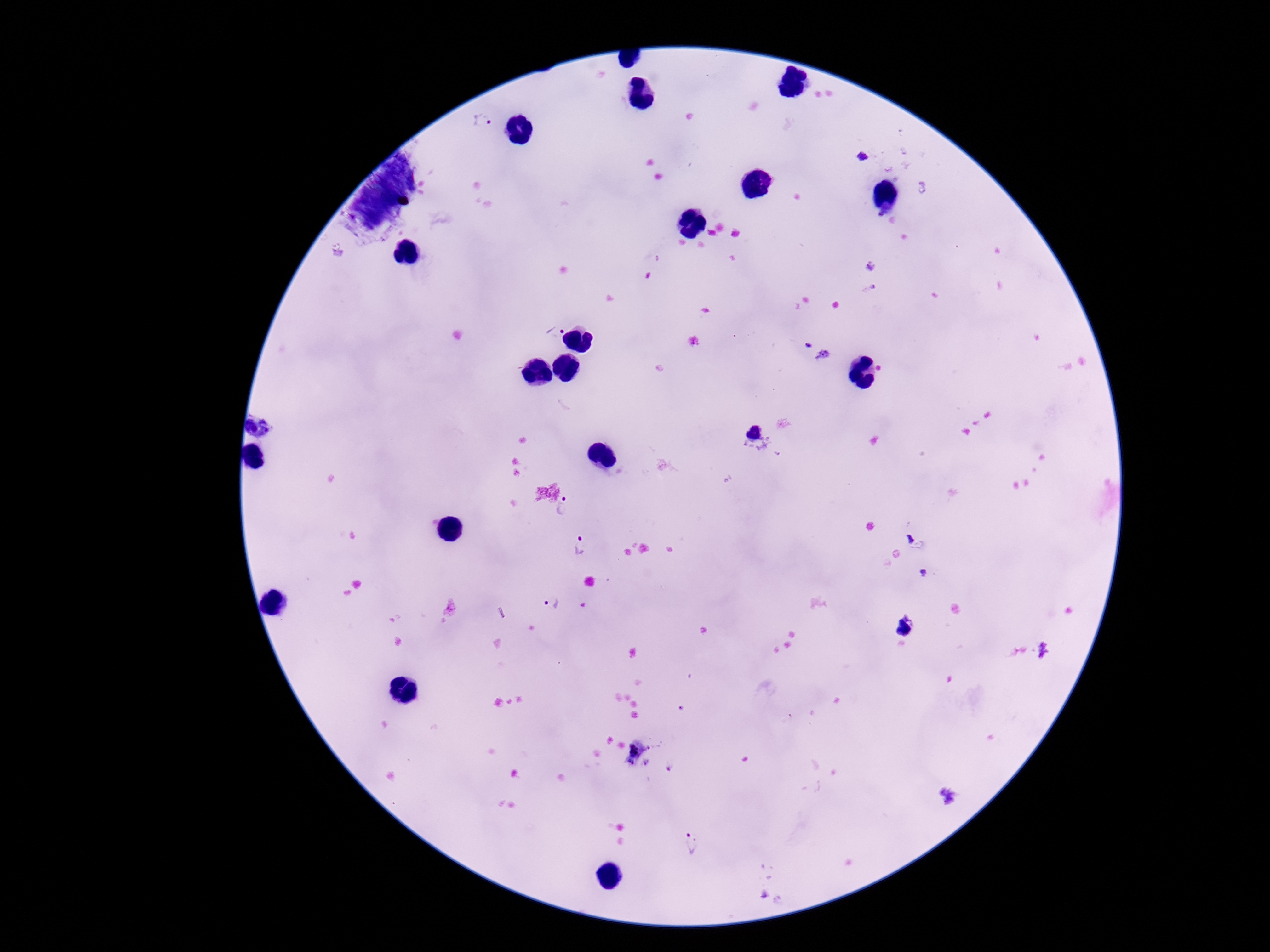

field of view = one from this slide
Plasmodium parasite locations = approximate object centers, in pixels from the top-left corner: (x=483, y=121), (x=862, y=156), (x=555, y=329), (x=806, y=345), (x=564, y=506), (x=581, y=548), (x=552, y=603), (x=632, y=752), (x=945, y=794), (x=692, y=844)
preparation = thick peripheral-blood smear
patient malaria status = infected
image size = 1270×952 pixels
capture = smartphone camera through the microscope eyepiece
magnification = 100x
stain = Giemsa